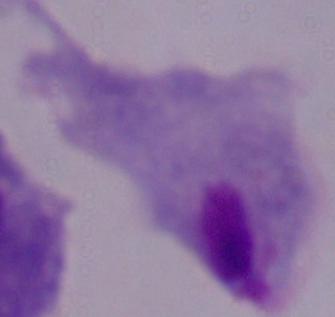 1000x magnification. A trichomonad is seen. Photomicrograph.